State which parasite is depicted.
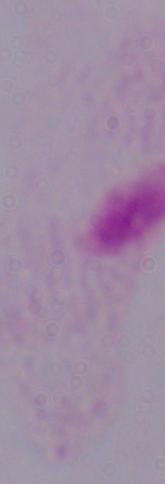

This is a trichomonad.

Micrograph. 1000x magnification.